Point out each Plasmodium parasite.
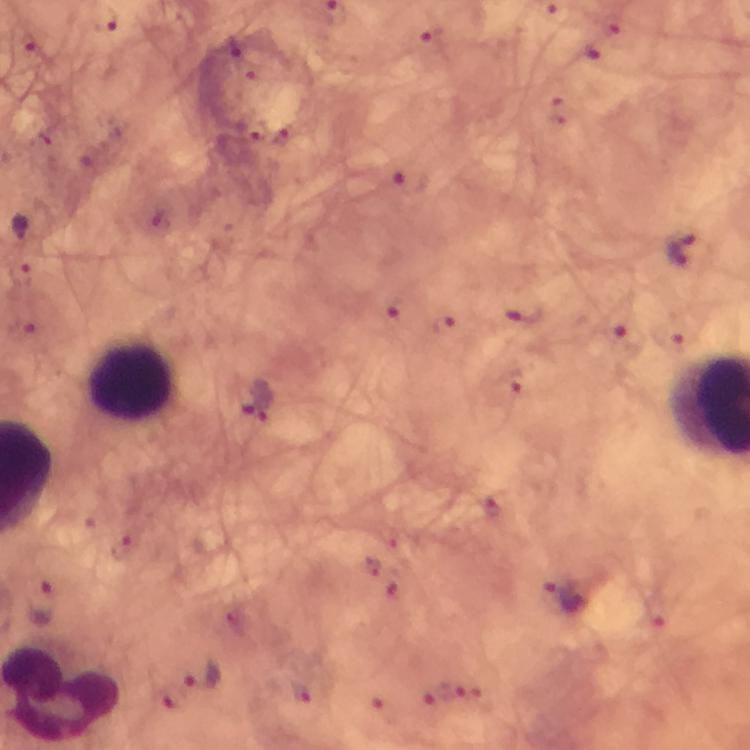

Approximate centers as (x, y) in pixels.
Plasmodium parasites: (102, 19), (408, 183), (19, 228), (679, 250), (255, 400), (564, 596), (43, 604), (202, 675).

Summary:
  - Leukocyte locations: (132, 382)
  - Image size: 750×750 pixels
  - Context: from a diagnostic examination for malaria
  - Stain: Giemsa
  - Capture: smartphone photograph through a microscope
  - Immersion oil: applied
  - Preparation: thick smear
  - Cropped from: one field of view
  - Magnification: 100x